Report the malaria status of this cell.
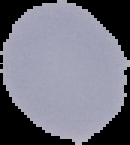
Uninfected.

preparation = thin blood smear
image size = 130×145 pixels
image type = segmented cell region on a black background